State which parasite is depicted.
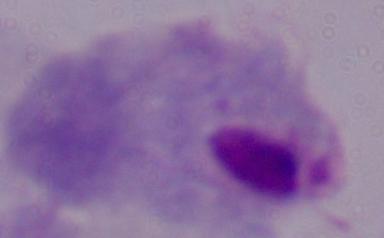

This is a trichomonad.

Summary:
  - Magnification: 1000x
  - Modality: micrograph